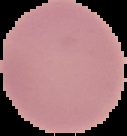

Segmented cell region on a black background. Malaria status: uninfected. Image is 127×136 pixels. From a thin blood smear.